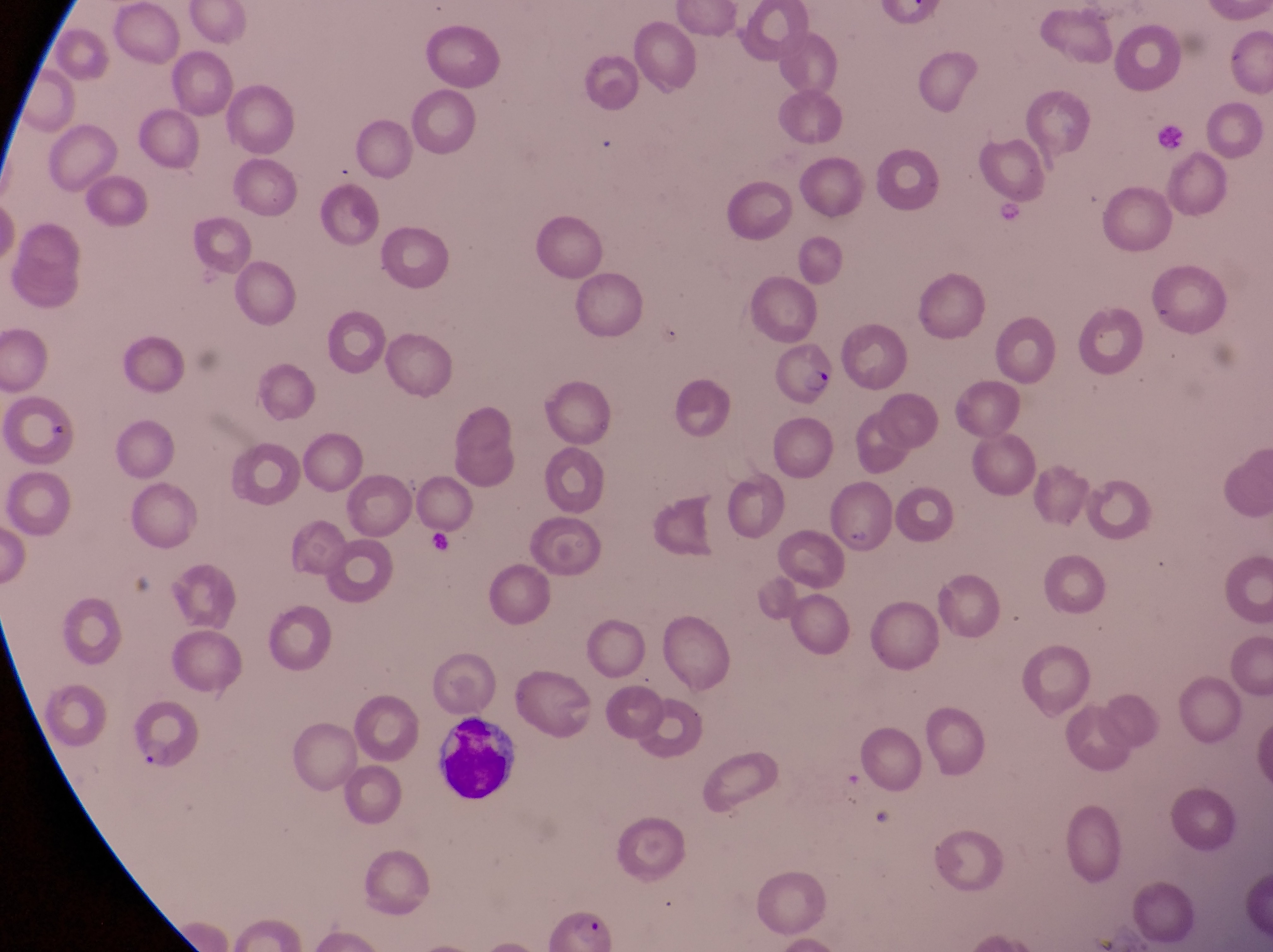

magnification = 1000x
parasitised red blood cell locations = approximate bounding boxes as left top right bottom in pixels: 774 342 837 412; 828 487 903 562; 128 702 202 772
capture = smartphone photograph through the eyepiece of an Olympus CX-23 microscope
country = Uganda
artifact (platelet-like body, stain precipitate, or debris) locations = approximate bounding boxes as left top right bottom in pixels: 430 719 518 804
preparation = thin blood film
field of view = single
image size = 1273×952 pixels